Report the malaria status of this cell.
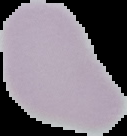

Uninfected.

Cell region segmented out of the field of view; the surrounding area is masked to black. From a thin blood smear. Image is 127×136 pixels.